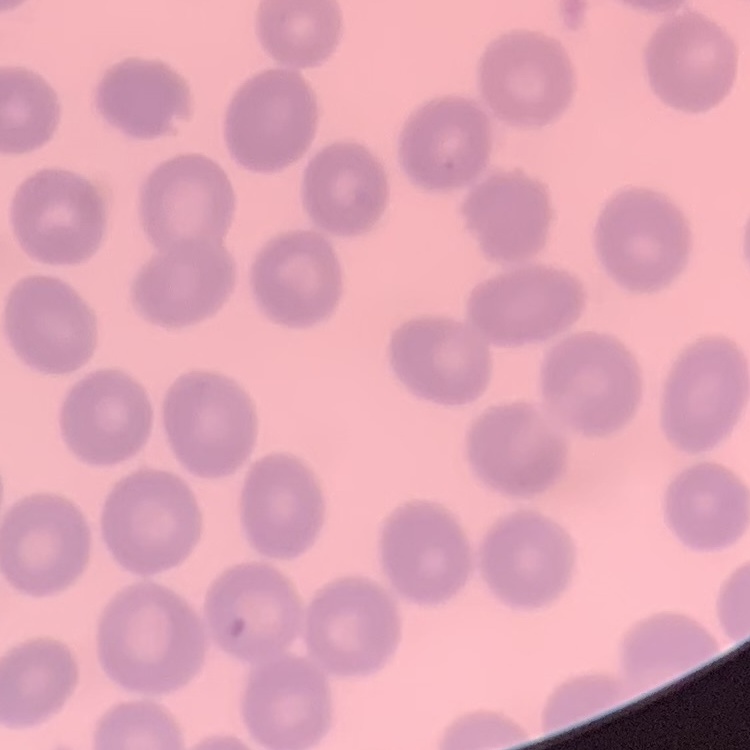
erythrocyte morphology = no rouleaux formation
preparation = thin peripheral smear
stain = Field's or Giemsa
image type = square crop of a larger photomicrograph